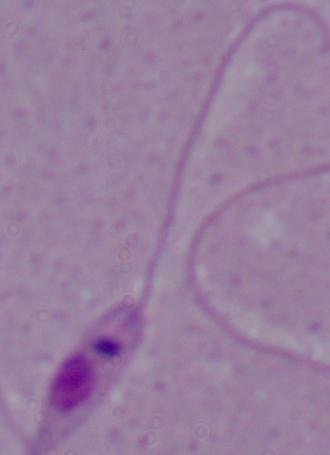

magnification = 1000x
identification = Leishmania
modality = photomicrograph